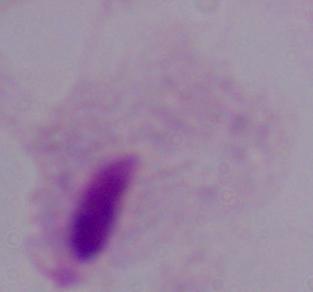
identification = trichomonad
magnification = 1000x
modality = photomicrograph